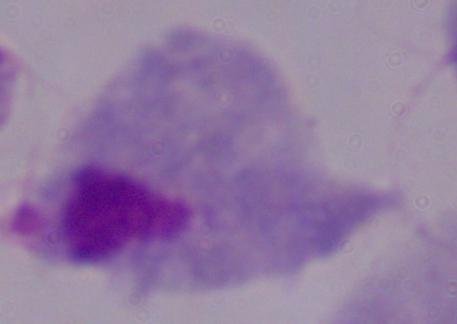
Summary:
  - Magnification: 1000x
  - Modality: micrograph
  - Identification: trichomonad